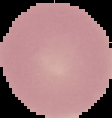
Summary:
  - Image type: cell region segmented out of the field of view; surrounding area masked to black
  - Preparation: thin blood film
  - Result: negative for Plasmodium parasites
  - Image size: 112×118 pixels